Assess this cell for malaria.
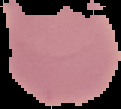
It is uninfected.

Summary:
  - Image size: 121×109 pixels
  - Image type: cell region segmented out of the field of view; surrounding area masked to black
  - Preparation: thin blood film